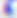
Toxoplasma gondii is shown. Micrograph. 400x magnification.